Identify the parasite.
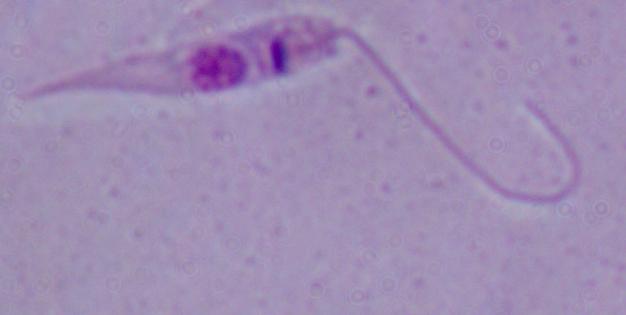

This is Leishmania.

magnification = 1000x
modality = micrograph